Classify this cell by malaria status.
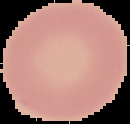

Uninfected.

Summary:
  - Image size: 130×124 pixels
  - Preparation: thin blood film
  - Image type: cell region segmented out of the field of view; surrounding area masked to black